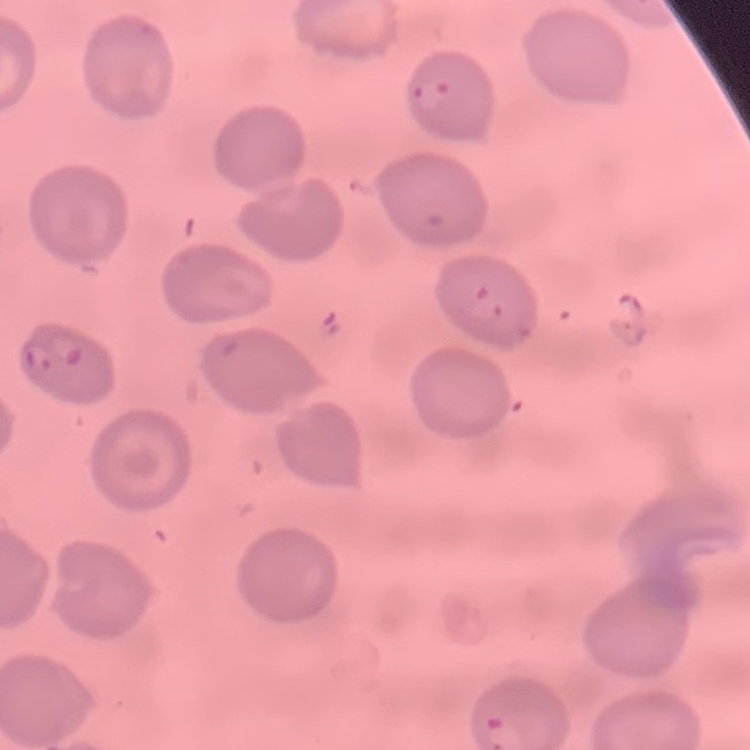
The erythrocytes exhibit no rouleaux formation. One tile cut from a larger photomicrograph. Field's or Giemsa stain. Thin peripheral smear.